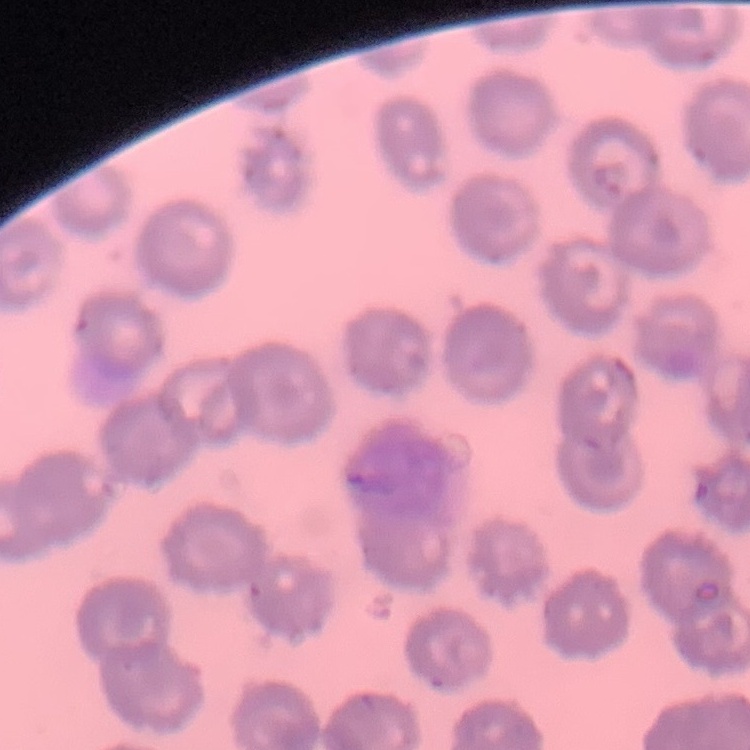
The erythrocytes exhibit no rouleaux formation. Thin blood smear. Square crop of a larger photomicrograph. Stained with either Field's or Giemsa.